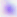
Captured at 400x magnification. Micrograph. Toxoplasma gondii is seen.